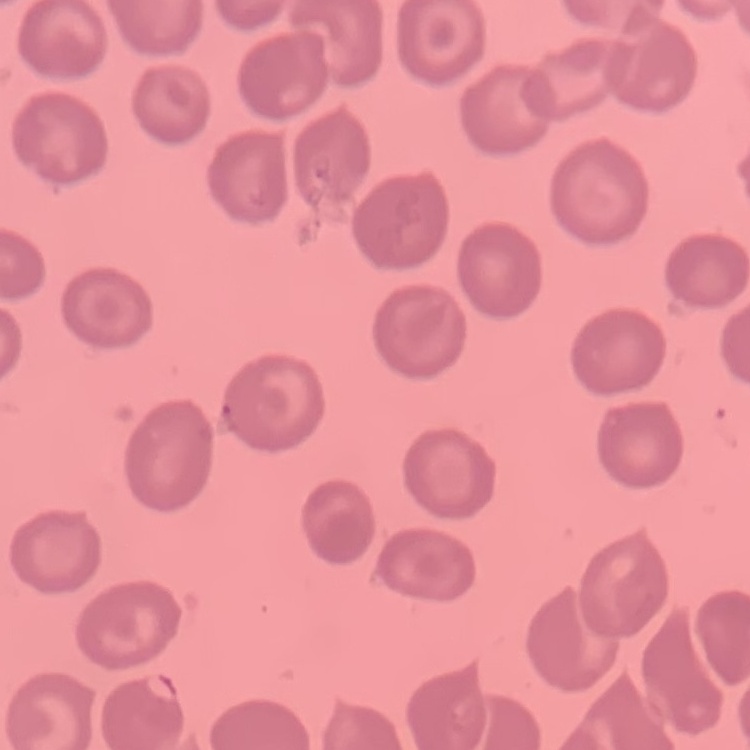
The red blood cells show no rouleaux formation. Square crop of a larger photomicrograph. Stained with either Field's or Giemsa. Thin peripheral smear.